Identify the blood parasite species.
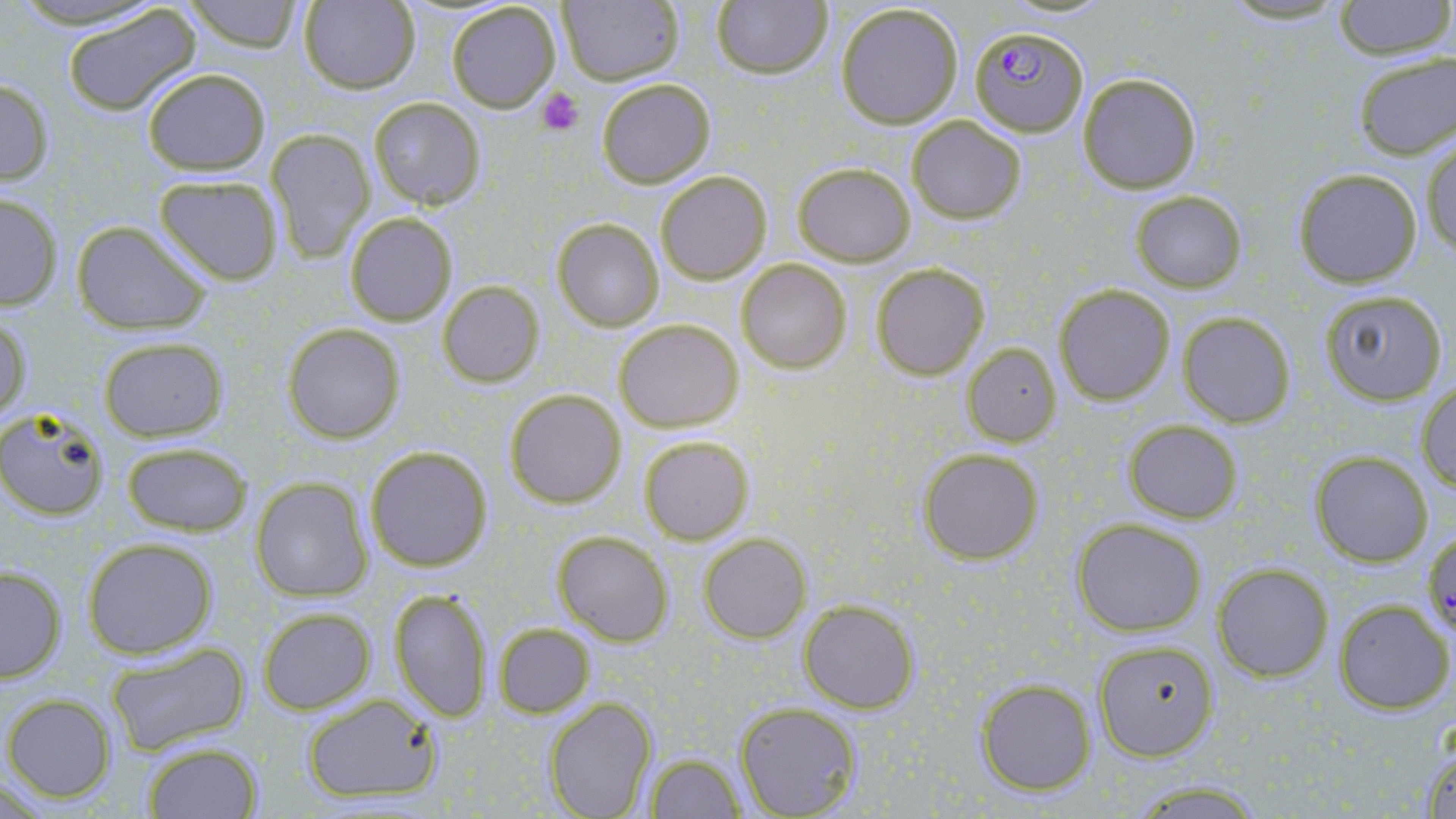
Plasmodium falciparum.

magnification = 1000x
field of view = one of a larger specimen
uninfected red blood cell locations = approximate bounding boxes as (x1, y1, x2, y2) in pixels: (7, 0, 170, 30), (182, 0, 304, 52), (557, 0, 683, 86), (711, 0, 832, 79), (1214, 0, 1355, 27), (1332, 0, 1455, 60), (298, 1, 421, 94), (447, 2, 561, 112), (834, 2, 966, 129), (63, 3, 201, 115), (1351, 51, 1455, 161), (142, 68, 270, 174), (1077, 73, 1202, 193), (0, 76, 54, 186), (596, 77, 717, 188), (369, 97, 486, 208), (906, 114, 1028, 225), (266, 128, 373, 262), (1422, 139, 1456, 260), (792, 162, 916, 266), (1292, 168, 1423, 287), (655, 171, 773, 284), (154, 174, 284, 285), (1129, 191, 1247, 292), (0, 193, 61, 308), (344, 211, 458, 326), (553, 219, 663, 331), (71, 220, 210, 335), (735, 259, 853, 373), (871, 263, 989, 380), (437, 281, 545, 387), (1055, 284, 1175, 405), (1317, 288, 1449, 406), (1177, 312, 1297, 427), (1, 315, 32, 425), (613, 318, 744, 433), (284, 323, 405, 443), (98, 336, 228, 441), (964, 344, 1062, 443), (1415, 381, 1456, 491), (505, 388, 627, 508), (0, 406, 111, 521), (1124, 421, 1243, 523), (637, 433, 755, 545), (120, 441, 254, 536), (364, 445, 493, 572), (917, 447, 1044, 565), (1308, 451, 1434, 567), (251, 478, 374, 602), (1071, 518, 1207, 636), (552, 530, 672, 645), (699, 533, 810, 643), (82, 537, 218, 658), (0, 564, 67, 682), (1211, 565, 1333, 681), (388, 588, 495, 721), (1333, 599, 1452, 714), (800, 601, 919, 713), (257, 607, 376, 714), (493, 622, 596, 718), (1092, 638, 1219, 760), (103, 642, 249, 756), (977, 678, 1096, 795), (301, 694, 445, 806), (4, 695, 116, 802), (544, 697, 658, 818), (733, 702, 861, 818), (142, 742, 263, 818), (1418, 743, 1456, 819), (644, 752, 746, 818), (1120, 779, 1269, 816)
preparation = thin blood film
Plasmodium falciparum-infected red blood cell locations = approximate bounding boxes as (x1, y1, x2, y2) in pixels: (969, 25, 1088, 136)
image size = 1456×819 pixels
modality = optical microscopy
stain = May-Grünwald-Giemsa
platelet locations = approximate bounding boxes as (x1, y1, x2, y2) in pixels: (536, 87, 583, 135)